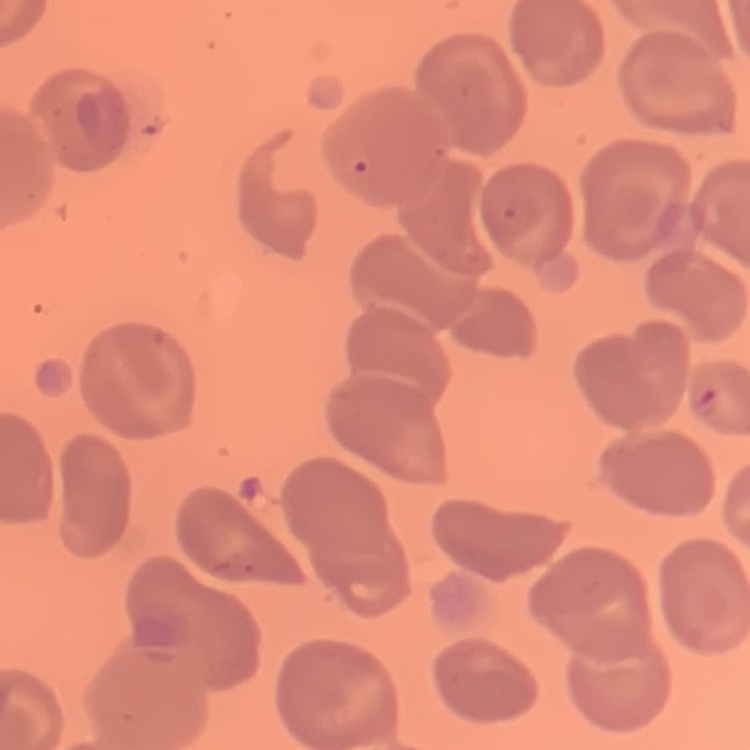

Summary:
  - Erythrocyte morphology: no rouleaux formation
  - Stain: Field's or Giemsa
  - Preparation: thin blood smear
  - Image type: square crop of a larger photomicrograph